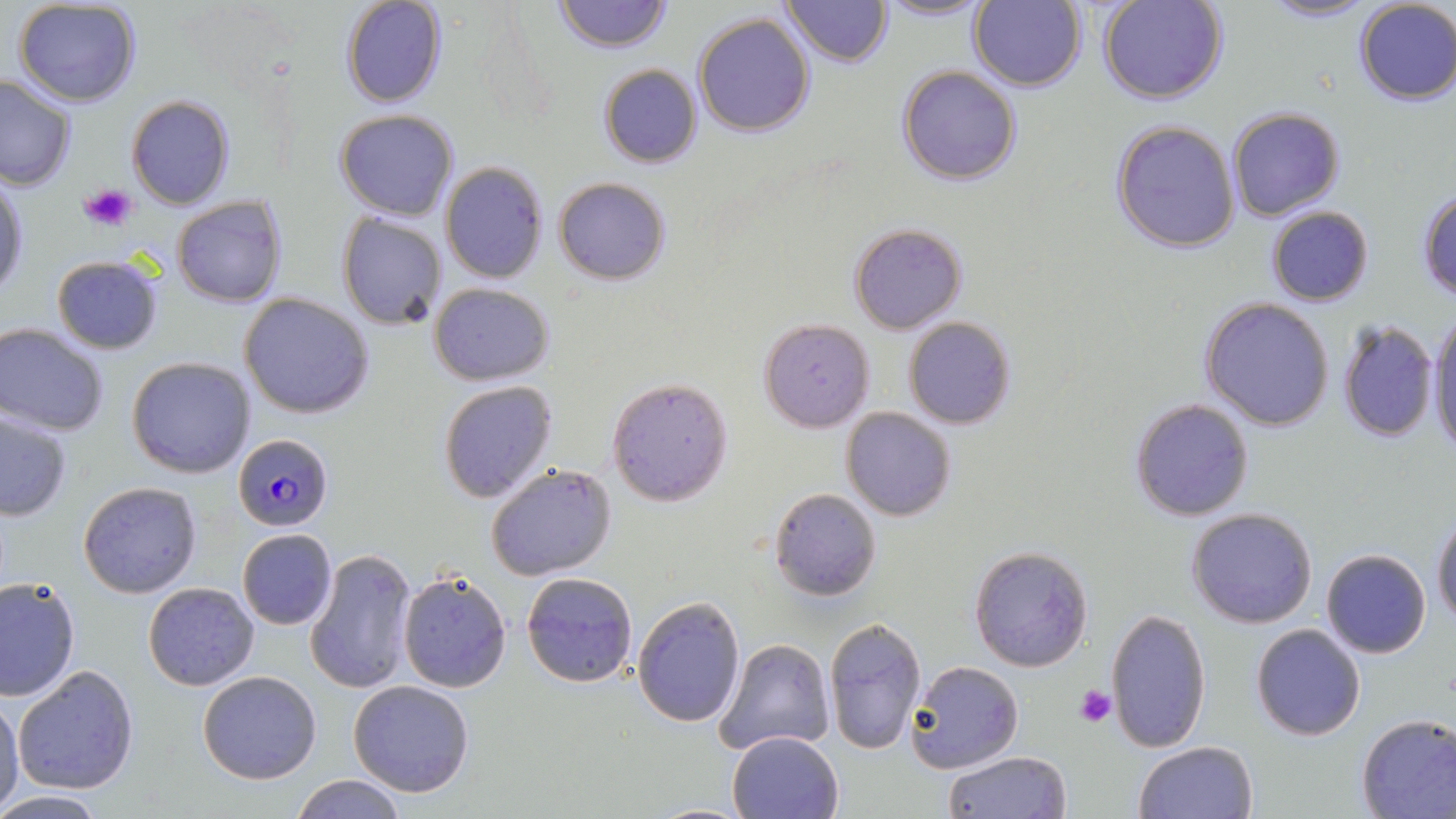

Approximate bounding boxes as named x1/y1/x2/y2 corners in pixels. Plasmodium falciparum-infected red blood cell locations: (x1=232, y1=433, x2=334, y2=531). Platelet locations: (x1=80, y1=181, x2=139, y2=234), (x1=1074, y1=685, x2=1116, y2=728). Uninfected red blood cell locations: (x1=340, y1=0, x2=447, y2=108), (x1=554, y1=0, x2=672, y2=53), (x1=782, y1=0, x2=893, y2=68), (x1=1098, y1=0, x2=1228, y2=105), (x1=1259, y1=0, x2=1379, y2=23), (x1=12, y1=1, x2=143, y2=108), (x1=874, y1=1, x2=990, y2=21), (x1=969, y1=1, x2=1089, y2=93), (x1=1353, y1=1, x2=1455, y2=107), (x1=692, y1=12, x2=817, y2=137), (x1=599, y1=64, x2=702, y2=168), (x1=895, y1=65, x2=1022, y2=184), (x1=0, y1=73, x2=76, y2=191), (x1=125, y1=95, x2=235, y2=210), (x1=1226, y1=106, x2=1345, y2=222), (x1=334, y1=109, x2=460, y2=222), (x1=1111, y1=120, x2=1241, y2=253), (x1=439, y1=162, x2=548, y2=284), (x1=1, y1=176, x2=29, y2=299), (x1=554, y1=177, x2=671, y2=285), (x1=1416, y1=189, x2=1456, y2=300), (x1=171, y1=195, x2=288, y2=307), (x1=1266, y1=206, x2=1374, y2=306), (x1=336, y1=210, x2=448, y2=331), (x1=847, y1=222, x2=968, y2=335), (x1=50, y1=254, x2=165, y2=355), (x1=429, y1=282, x2=554, y2=383), (x1=239, y1=293, x2=375, y2=419), (x1=1200, y1=297, x2=1336, y2=431), (x1=1427, y1=309, x2=1456, y2=456), (x1=902, y1=316, x2=1016, y2=428), (x1=758, y1=317, x2=875, y2=431), (x1=1337, y1=318, x2=1439, y2=441), (x1=0, y1=322, x2=110, y2=435), (x1=126, y1=355, x2=256, y2=478), (x1=606, y1=375, x2=734, y2=506), (x1=438, y1=379, x2=560, y2=503), (x1=1129, y1=397, x2=1255, y2=521), (x1=841, y1=407, x2=958, y2=522), (x1=0, y1=410, x2=73, y2=521), (x1=485, y1=463, x2=618, y2=582), (x1=77, y1=481, x2=203, y2=599), (x1=768, y1=488, x2=880, y2=602), (x1=1187, y1=508, x2=1317, y2=628), (x1=1431, y1=512, x2=1456, y2=626), (x1=237, y1=529, x2=336, y2=630), (x1=968, y1=544, x2=1094, y2=670), (x1=301, y1=547, x2=417, y2=695), (x1=1321, y1=549, x2=1432, y2=658), (x1=398, y1=571, x2=513, y2=691), (x1=519, y1=571, x2=639, y2=688), (x1=0, y1=578, x2=81, y2=702), (x1=143, y1=582, x2=261, y2=690), (x1=631, y1=594, x2=745, y2=727), (x1=1104, y1=607, x2=1213, y2=751), (x1=823, y1=615, x2=928, y2=756), (x1=1250, y1=623, x2=1366, y2=742), (x1=712, y1=636, x2=837, y2=756), (x1=908, y1=660, x2=1024, y2=774), (x1=12, y1=665, x2=140, y2=794), (x1=197, y1=671, x2=322, y2=785), (x1=347, y1=680, x2=475, y2=799), (x1=0, y1=695, x2=24, y2=813), (x1=1354, y1=714, x2=1456, y2=819), (x1=727, y1=729, x2=842, y2=818), (x1=1134, y1=740, x2=1260, y2=819), (x1=943, y1=750, x2=1072, y2=819), (x1=289, y1=774, x2=408, y2=818), (x1=0, y1=792, x2=112, y2=817). Slide-level diagnosis: Plasmodium falciparum. Optical microscopy. May-Grünwald-Giemsa-stained preparation. Captured at 1000x magnification. Image is 1456×819 pixels. Single field of view. Thin blood film.